Report the malaria status of this cell.
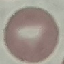
Uninfected.

Summary:
  - Stain: Giemsa
  - Capture: smartphone through the microscope eyepiece
  - Image type: cell patch, automatically extracted from a larger field of view and resized to 64 × 64 pixels
  - Preparation: thin blood smear